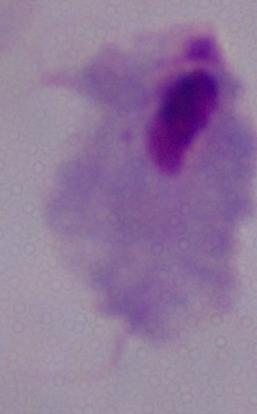
Summary:
  - Magnification: 1000x
  - Identification: trichomonad
  - Modality: micrograph